State which parasite is depicted.
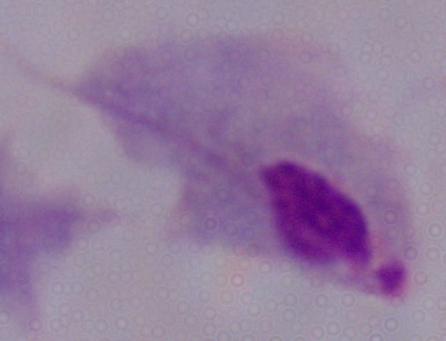
This is a trichomonad.

Summary:
  - Magnification: 1000x
  - Modality: micrograph